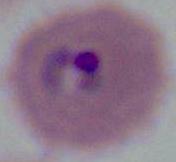
400x or 1000x magnification. A Plasmodium parasite is shown. Photomicrograph.